Draw a bounding box around every leukocyte (white blood cell).
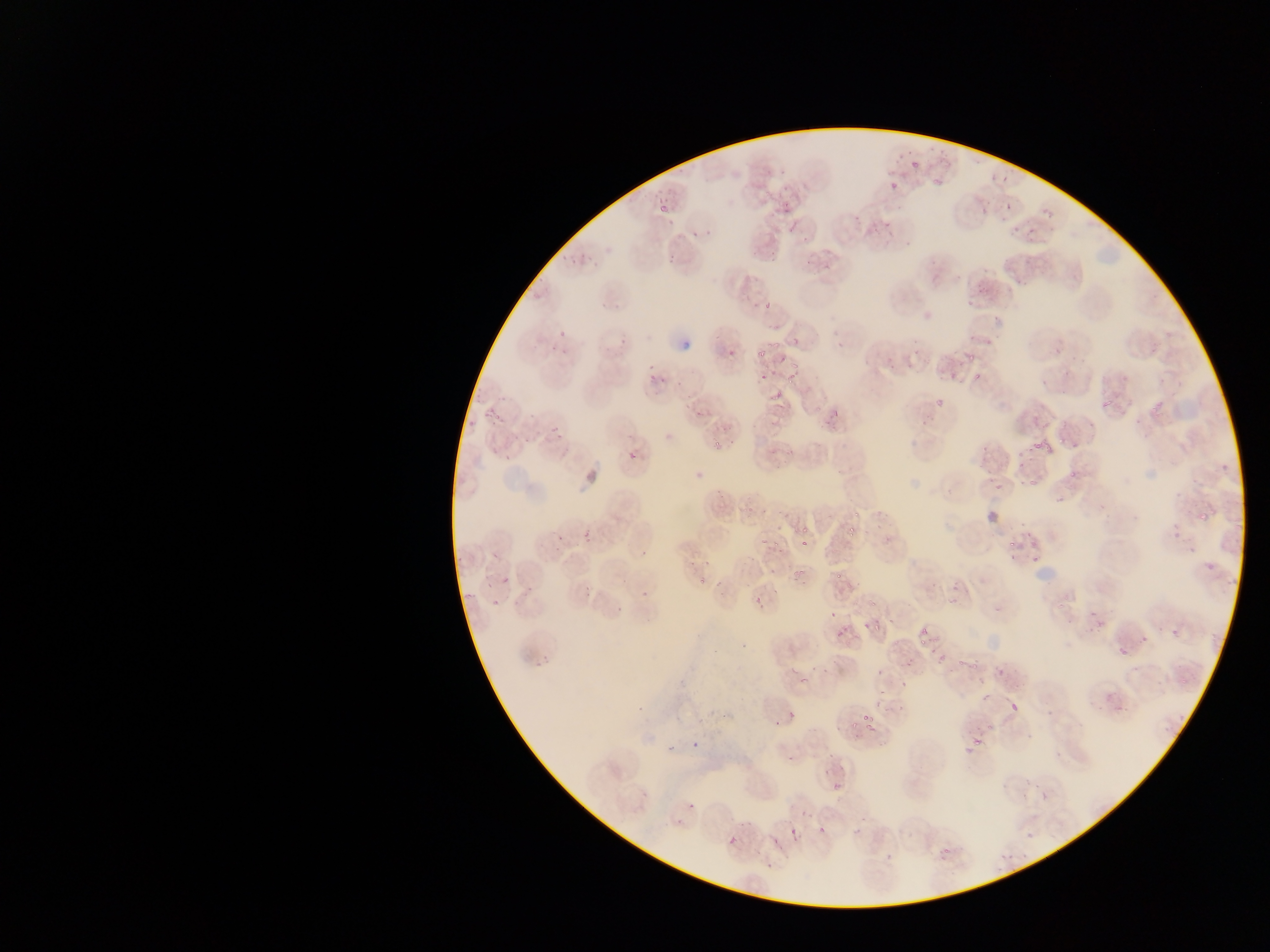
No leukocytes observed.

Approximate bounding boxes as (left, top, right, bottom) in pixels. Plasmodium parasite locations: (909, 154, 923, 170), (885, 181, 896, 195), (779, 186, 796, 212), (1002, 197, 1016, 211), (655, 203, 672, 221), (977, 205, 987, 219), (851, 212, 863, 226), (1041, 212, 1053, 218), (1010, 227, 1023, 238), (689, 228, 701, 241), (767, 236, 784, 259), (663, 253, 680, 263), (803, 258, 813, 265), (758, 301, 773, 311), (550, 324, 586, 343), (791, 335, 802, 344), (680, 338, 693, 352), (773, 338, 777, 354), (834, 340, 848, 347), (721, 342, 737, 356), (756, 345, 769, 360), (965, 345, 983, 363), (777, 352, 789, 366), (790, 361, 797, 373), (946, 366, 958, 381), (757, 371, 774, 381), (784, 371, 800, 384), (970, 373, 984, 381), (654, 375, 670, 385), (772, 382, 786, 394), (933, 387, 947, 409), (483, 401, 499, 421), (1098, 401, 1114, 408), (826, 405, 846, 427), (1148, 406, 1159, 414), (548, 424, 565, 442), (662, 431, 679, 437), (1057, 436, 1065, 446), (1029, 438, 1041, 448), (712, 440, 723, 449), (1046, 440, 1053, 452), (983, 443, 994, 460), (625, 447, 641, 465), (1000, 450, 1014, 467), (1017, 458, 1026, 468), (692, 465, 704, 479), (1068, 470, 1078, 479), (993, 477, 1008, 491), (1028, 479, 1038, 486), (1191, 501, 1210, 526), (981, 506, 1005, 530), (851, 508, 861, 518), (843, 526, 861, 540), (1166, 526, 1179, 543), (799, 528, 809, 532), (556, 531, 566, 543), (578, 531, 596, 543), (885, 533, 894, 543), (799, 537, 811, 551), (1003, 537, 1020, 552), (771, 538, 780, 549), (638, 539, 651, 558), (758, 539, 765, 548), (1031, 547, 1039, 564), (1200, 555, 1210, 569), (790, 567, 804, 582), (833, 567, 849, 578), (497, 572, 513, 589), (692, 575, 706, 587), (520, 587, 530, 605), (581, 587, 594, 597), (748, 590, 766, 608), (639, 591, 651, 599), (947, 593, 961, 604), (489, 597, 503, 612), (869, 597, 880, 608), (1054, 600, 1064, 613), (827, 604, 840, 620), (613, 608, 629, 614), (863, 617, 880, 633), (1095, 620, 1107, 633), (919, 623, 927, 637), (835, 625, 849, 639), (1169, 626, 1184, 642), (916, 638, 926, 646), (1112, 640, 1134, 663), (929, 646, 947, 663), (533, 653, 550, 669), (900, 654, 914, 664), (970, 658, 980, 675), (992, 664, 1008, 679), (799, 665, 810, 684), (872, 665, 882, 679), (895, 673, 912, 690), (972, 687, 989, 704), (873, 689, 881, 698), (1004, 696, 1026, 718), (895, 705, 901, 717), (787, 706, 801, 719), (862, 716, 874, 730), (849, 720, 859, 729), (775, 721, 782, 729), (968, 725, 981, 748), (1025, 732, 1034, 738), (691, 733, 704, 751), (667, 742, 676, 755), (785, 752, 799, 768), (1054, 752, 1064, 758), (1021, 775, 1033, 785), (830, 781, 844, 789), (638, 785, 651, 797), (1040, 792, 1052, 802), (686, 801, 697, 812), (787, 823, 799, 834), (817, 826, 828, 836), (1026, 834, 1035, 840), (727, 835, 740, 847), (774, 835, 781, 846), (936, 844, 955, 864), (763, 853, 777, 873), (883, 854, 895, 859) | approximate (x, y) pixel centers of objects too small to bound: (935, 183), (958, 663), (1005, 784), (677, 822), (1011, 854), (1003, 856), (999, 872). Collected in Ghana. Photographed through a microscope with a mobile-phone camera. Image is 1270×952 pixels. One field of view. Thin blood film.